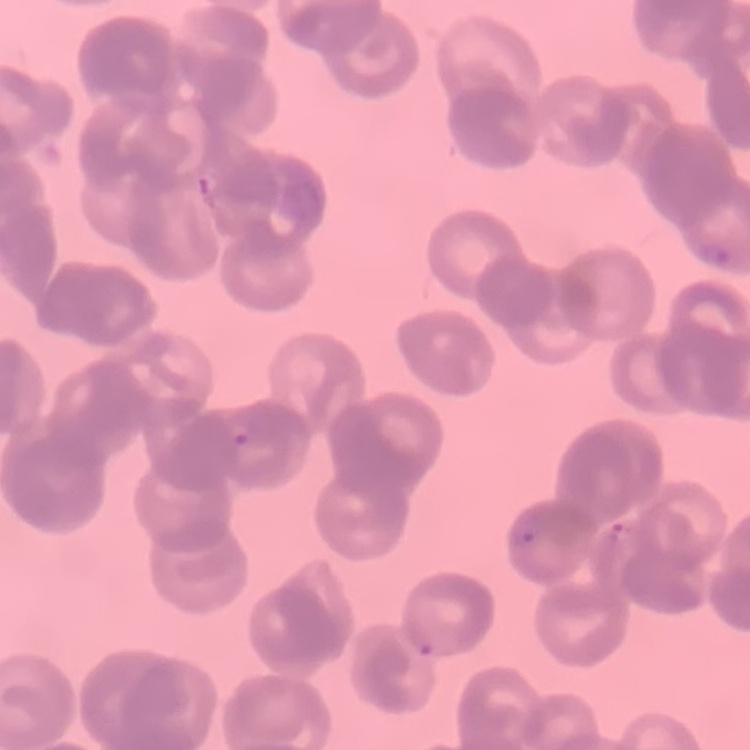

erythrocyte morphology = rouleaux formation
preparation = thin peripheral smear
image type = square crop of a larger photomicrograph
stain = Field's or Giemsa